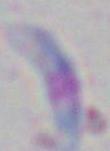
Summary:
  - Modality: micrograph
  - Identification: Toxoplasma gondii
  - Magnification: 1000x